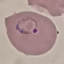
Result: malaria parasites identified. Cell patch, automatically extracted from a larger field of view and resized to 64 × 64 pixels. Giemsa stain. Thin smear of blood. Photographed with a smartphone camera at the microscope eyepiece.